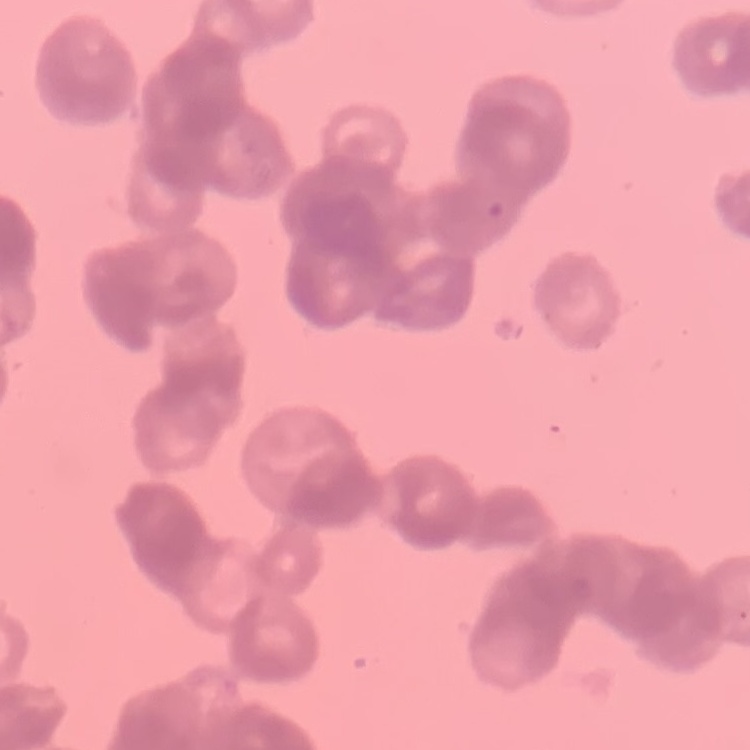
Summary:
  - Red blood cell morphology: rouleaux formation
  - Stain: Field's or Giemsa
  - Preparation: thin peripheral smear
  - Image type: one tile cut from a larger photomicrograph